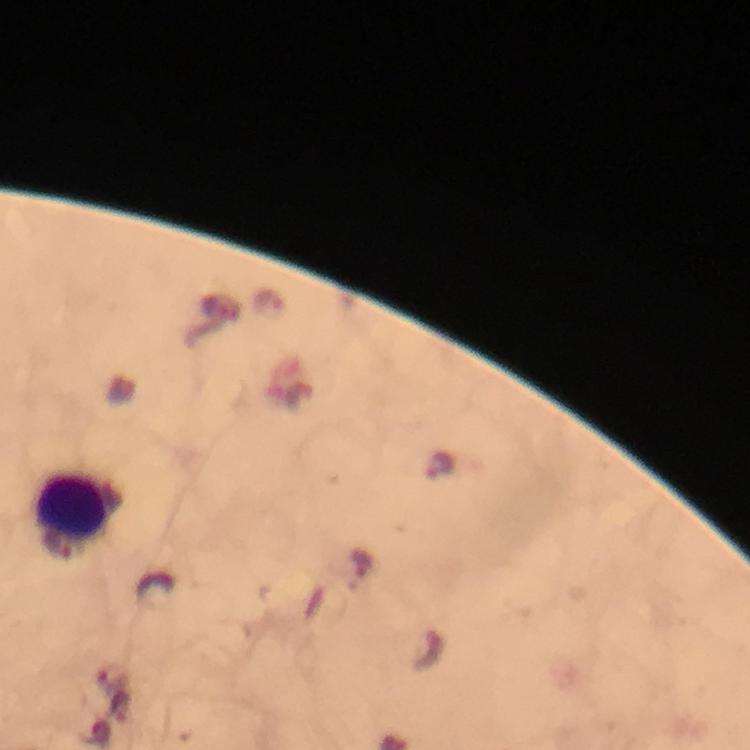 Approximate centers as (x, y) in pixels. Leukocyte locations: (74, 509). Plasmodium parasite locations: (441, 465). Giemsa-stained preparation. Thick blood smear. At 100x magnification. Image is 750×750 pixels. Immersion oil applied. From a malaria diagnostic workup. Smartphone photograph taken through a microscope. A crop from one field of view.